Locate every Plasmodium vivax-infected red blood cell.
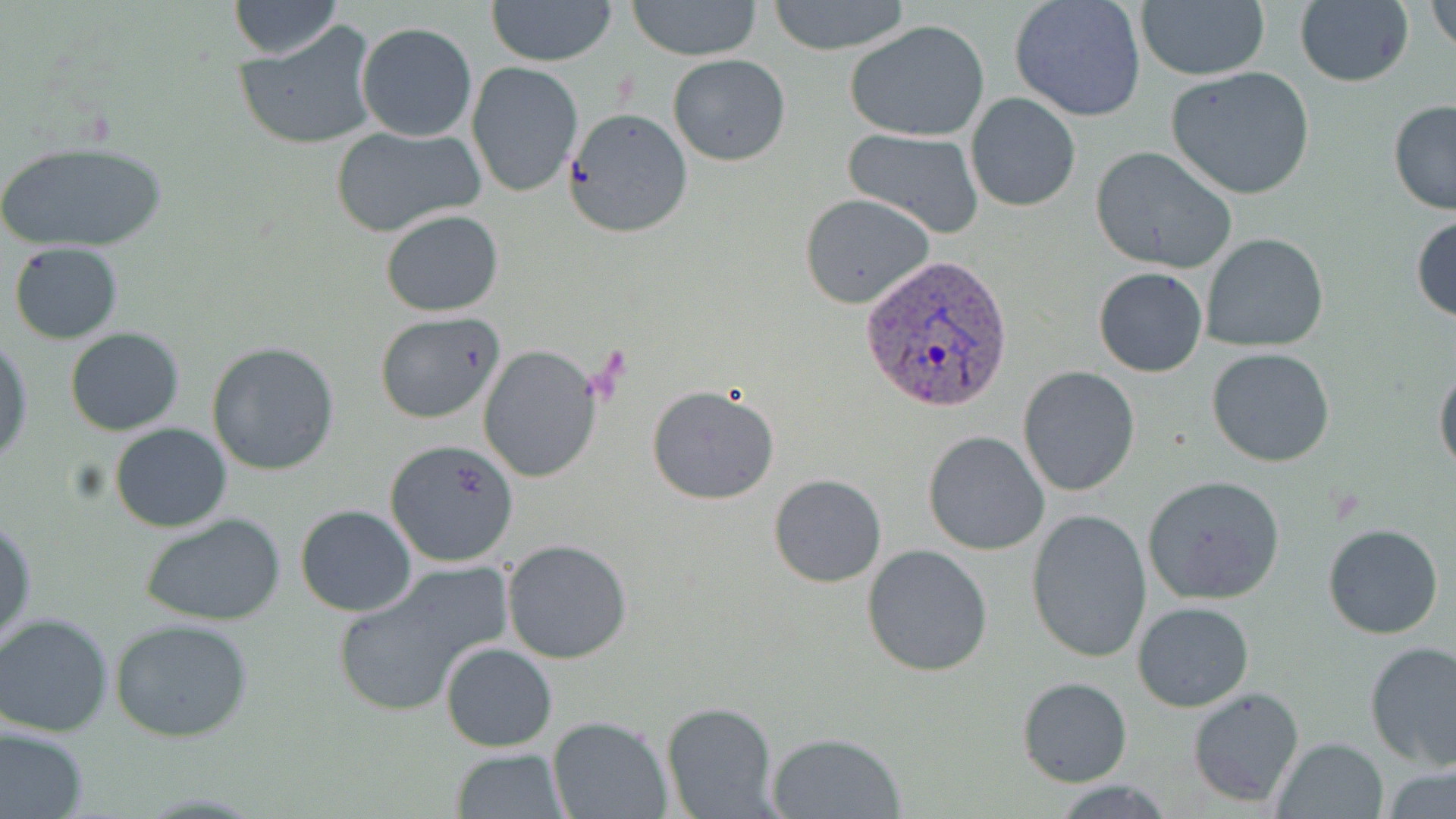

Approximate bounding boxes as named x1/y1/x2/y2 corners in pixels.
Plasmodium vivax-infected red blood cells: (x1=859, y1=255, x2=1012, y2=413).

Uninfected red blood cell locations: (x1=486, y1=0, x2=619, y2=67), (x1=627, y1=0, x2=764, y2=60), (x1=1010, y1=0, x2=1147, y2=123), (x1=227, y1=1, x2=343, y2=61), (x1=766, y1=1, x2=912, y2=54), (x1=1136, y1=1, x2=1270, y2=81), (x1=1294, y1=1, x2=1413, y2=87), (x1=1428, y1=1, x2=1456, y2=56), (x1=845, y1=19, x2=991, y2=142), (x1=234, y1=20, x2=381, y2=151), (x1=356, y1=22, x2=477, y2=141), (x1=667, y1=55, x2=790, y2=167), (x1=466, y1=61, x2=584, y2=197), (x1=1165, y1=67, x2=1316, y2=199), (x1=965, y1=92, x2=1080, y2=212), (x1=1387, y1=101, x2=1456, y2=216), (x1=564, y1=108, x2=693, y2=238), (x1=330, y1=124, x2=484, y2=237), (x1=844, y1=127, x2=986, y2=238), (x1=0, y1=139, x2=171, y2=257), (x1=1090, y1=146, x2=1238, y2=273), (x1=800, y1=192, x2=935, y2=309), (x1=380, y1=209, x2=504, y2=316), (x1=1411, y1=214, x2=1456, y2=325), (x1=1199, y1=232, x2=1329, y2=352), (x1=9, y1=243, x2=124, y2=344), (x1=1093, y1=266, x2=1208, y2=377), (x1=374, y1=312, x2=506, y2=425), (x1=65, y1=327, x2=184, y2=436), (x1=0, y1=336, x2=34, y2=465), (x1=207, y1=342, x2=340, y2=475), (x1=477, y1=345, x2=601, y2=483), (x1=1205, y1=345, x2=1335, y2=467), (x1=1434, y1=365, x2=1456, y2=478), (x1=1018, y1=366, x2=1140, y2=496), (x1=646, y1=384, x2=781, y2=504), (x1=108, y1=422, x2=232, y2=533), (x1=923, y1=430, x2=1049, y2=555), (x1=384, y1=438, x2=521, y2=568), (x1=768, y1=473, x2=887, y2=587), (x1=1142, y1=475, x2=1285, y2=604), (x1=295, y1=504, x2=417, y2=616), (x1=1025, y1=508, x2=1150, y2=663), (x1=140, y1=511, x2=287, y2=627), (x1=1, y1=516, x2=36, y2=649), (x1=1323, y1=524, x2=1444, y2=640), (x1=502, y1=538, x2=633, y2=665), (x1=862, y1=545, x2=993, y2=677), (x1=331, y1=566, x2=500, y2=710), (x1=1133, y1=600, x2=1253, y2=712), (x1=0, y1=612, x2=118, y2=737), (x1=108, y1=617, x2=255, y2=742), (x1=1363, y1=641, x2=1456, y2=771), (x1=440, y1=642, x2=558, y2=752), (x1=1017, y1=677, x2=1133, y2=786), (x1=1186, y1=685, x2=1305, y2=808), (x1=660, y1=701, x2=779, y2=819), (x1=547, y1=715, x2=672, y2=819), (x1=0, y1=724, x2=89, y2=819), (x1=766, y1=731, x2=905, y2=817), (x1=1274, y1=736, x2=1387, y2=817), (x1=448, y1=747, x2=570, y2=818), (x1=1381, y1=766, x2=1456, y2=816), (x1=1050, y1=780, x2=1179, y2=816). Slide-level diagnosis: Plasmodium vivax. Light microscopy. Captured at 1000x magnification. Single field of view. Image is 1456×819 pixels. Thin blood film. May-Grünwald-Giemsa stain.